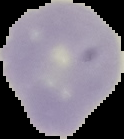
Malaria status: uninfected. From a thin blood film. Cell region segmented out of the field of view; the surrounding area is masked to black. Image is 124×139 pixels.